Assess this cell for malaria.
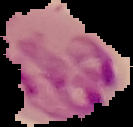

Parasitized.

Summary:
  - Preparation: thin blood smear
  - Image type: segmented cell region on a black background
  - Image size: 133×127 pixels